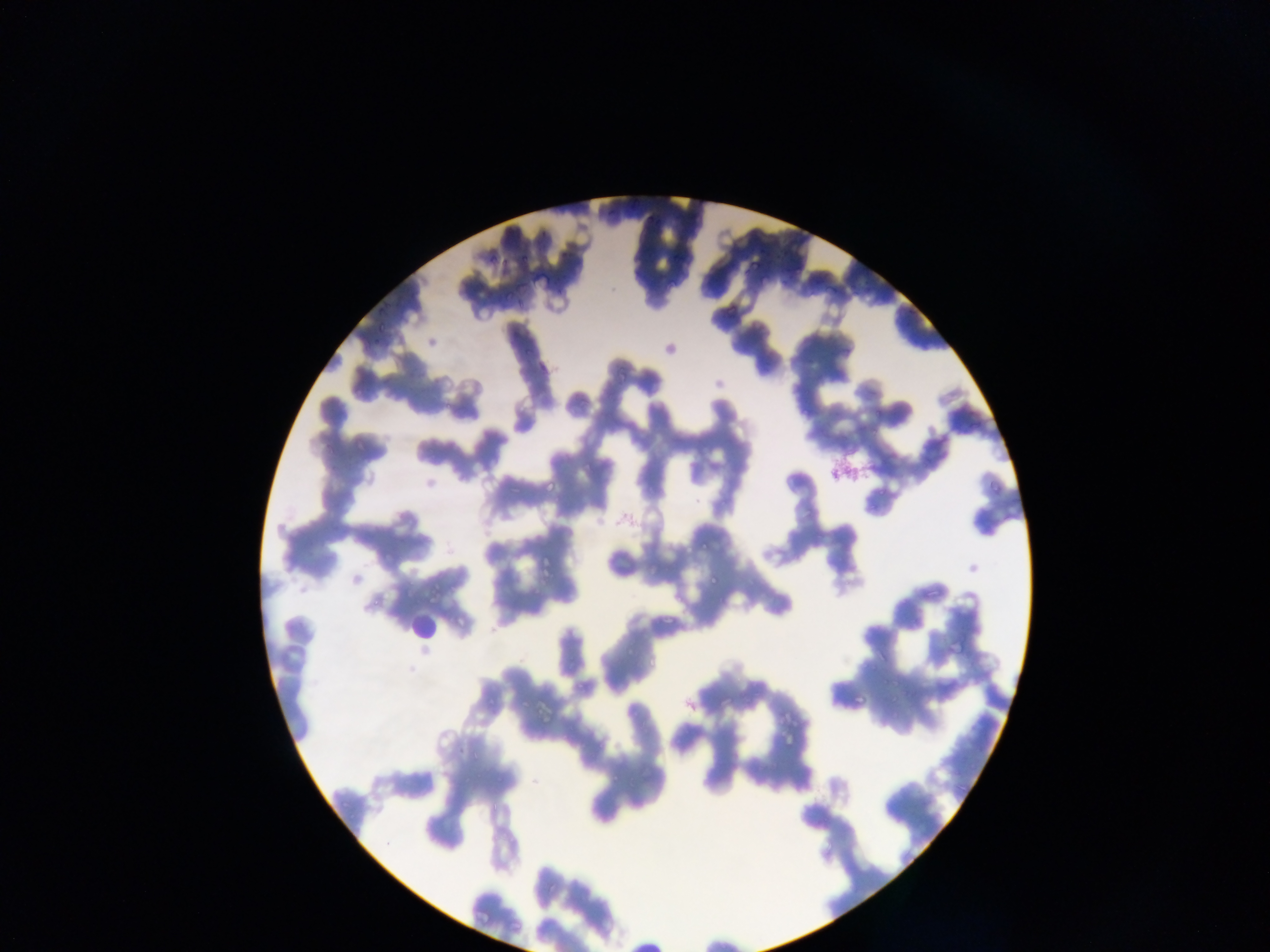
Approximate bounding boxes as {left, top, right, bottom} in pixels. Artifact (stain precipitate or debris) locations: {836, 446, 875, 482}. Malaria parasite locations: {604, 210, 617, 220}, {538, 227, 549, 236}, {756, 241, 775, 255}, {773, 246, 790, 260}, {487, 253, 498, 262}, {745, 255, 762, 274}, {519, 257, 529, 264}, {530, 275, 545, 285}, {822, 279, 836, 301}, {558, 285, 566, 298}, {503, 286, 517, 299}, {515, 301, 527, 311}, {903, 305, 918, 318}, {377, 306, 387, 313}, {376, 317, 389, 333}, {372, 337, 381, 343}, {525, 344, 537, 355}, {613, 362, 634, 381}, {544, 476, 564, 490}, {700, 536, 708, 549}, {539, 554, 554, 575}, {708, 571, 721, 586}, {663, 605, 680, 628}, {650, 654, 665, 669}, {852, 684, 871, 705}, {456, 744, 473, 753}. Leukocyte locations: {408, 597, 451, 643}. Collected in Ghana. Photographed through a microscope with a mobile-phone camera. Single field of view. Image is 1270×952 pixels. Thin blood film.